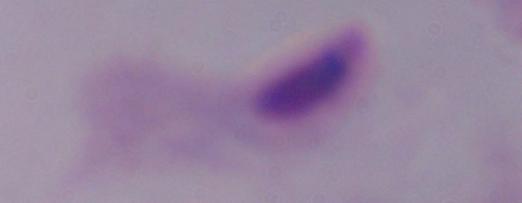 Photomicrograph. 1000x magnification. A trichomonad is seen.